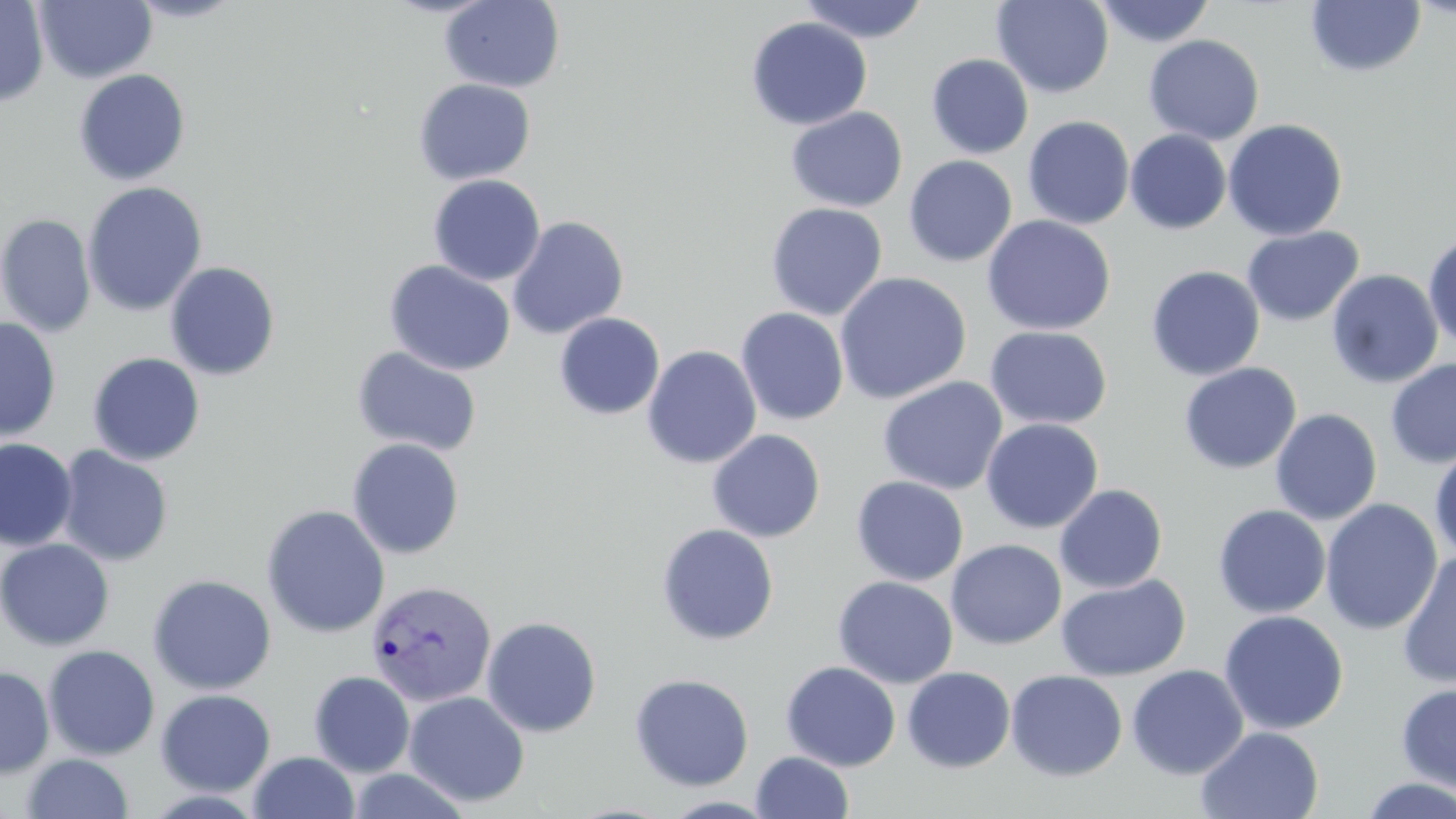
Summary:
  - Coordinate format: approximate bounding boxes as [x1, y1, x2, y2] in pixels
  - Plasmodium vivax-infected red blood cell locations: [365, 580, 496, 707]
  - Uninfected red blood cell locations: [0, 0, 49, 106], [35, 0, 157, 84], [125, 0, 246, 24], [440, 0, 565, 92], [992, 0, 1114, 98], [797, 1, 931, 43], [1093, 1, 1216, 48], [1305, 1, 1426, 78], [745, 16, 873, 131], [1143, 34, 1265, 145], [926, 53, 1033, 159], [73, 68, 191, 185], [413, 78, 536, 185], [785, 106, 908, 213], [1022, 116, 1135, 230], [1223, 118, 1348, 241], [1125, 130, 1231, 235], [904, 155, 1017, 267], [428, 174, 546, 286], [82, 182, 207, 317], [765, 202, 888, 321], [0, 214, 97, 337], [982, 215, 1116, 335], [507, 216, 629, 339], [1241, 225, 1364, 327], [1423, 233, 1456, 351], [384, 260, 516, 376], [165, 261, 281, 380], [1146, 265, 1265, 381], [1326, 269, 1444, 389], [834, 271, 972, 405], [736, 301, 972, 419], [735, 307, 849, 426], [554, 312, 665, 420], [0, 315, 61, 442], [984, 325, 1113, 430], [642, 345, 762, 468], [351, 346, 483, 457], [87, 352, 206, 466], [1385, 358, 1456, 469], [1179, 362, 1302, 474], [876, 376, 1009, 495], [1270, 408, 1383, 525], [981, 418, 1103, 534], [707, 429, 826, 543], [0, 438, 78, 551], [347, 438, 465, 559], [55, 445, 174, 566], [1429, 446, 1456, 561], [851, 476, 968, 586], [1054, 483, 1168, 594], [1320, 498, 1443, 636], [261, 504, 390, 638], [1212, 505, 1331, 618], [656, 523, 779, 645], [0, 538, 115, 650], [946, 539, 1066, 650], [1397, 552, 1456, 689], [147, 574, 277, 695], [1056, 574, 1191, 682], [832, 575, 958, 689], [1218, 610, 1349, 736], [480, 616, 602, 737], [43, 645, 160, 760], [781, 661, 901, 771], [1126, 664, 1248, 779], [0, 665, 55, 779], [902, 667, 1016, 772], [1005, 670, 1128, 781], [309, 671, 415, 777], [629, 673, 754, 791], [1395, 682, 1456, 793], [156, 689, 276, 796], [403, 691, 530, 808], [1196, 726, 1323, 819], [249, 751, 360, 819], [751, 751, 854, 819], [21, 753, 134, 818], [1355, 776, 1456, 818]
  - Slide-level diagnosis: Plasmodium vivax
  - Stain: May-Grünwald-Giemsa
  - Magnification: 1000x
  - Modality: optical microscopy
  - Field of view: single
  - Image size: 1456×819 pixels
  - Preparation: thin blood smear